Name the blood parasite species.
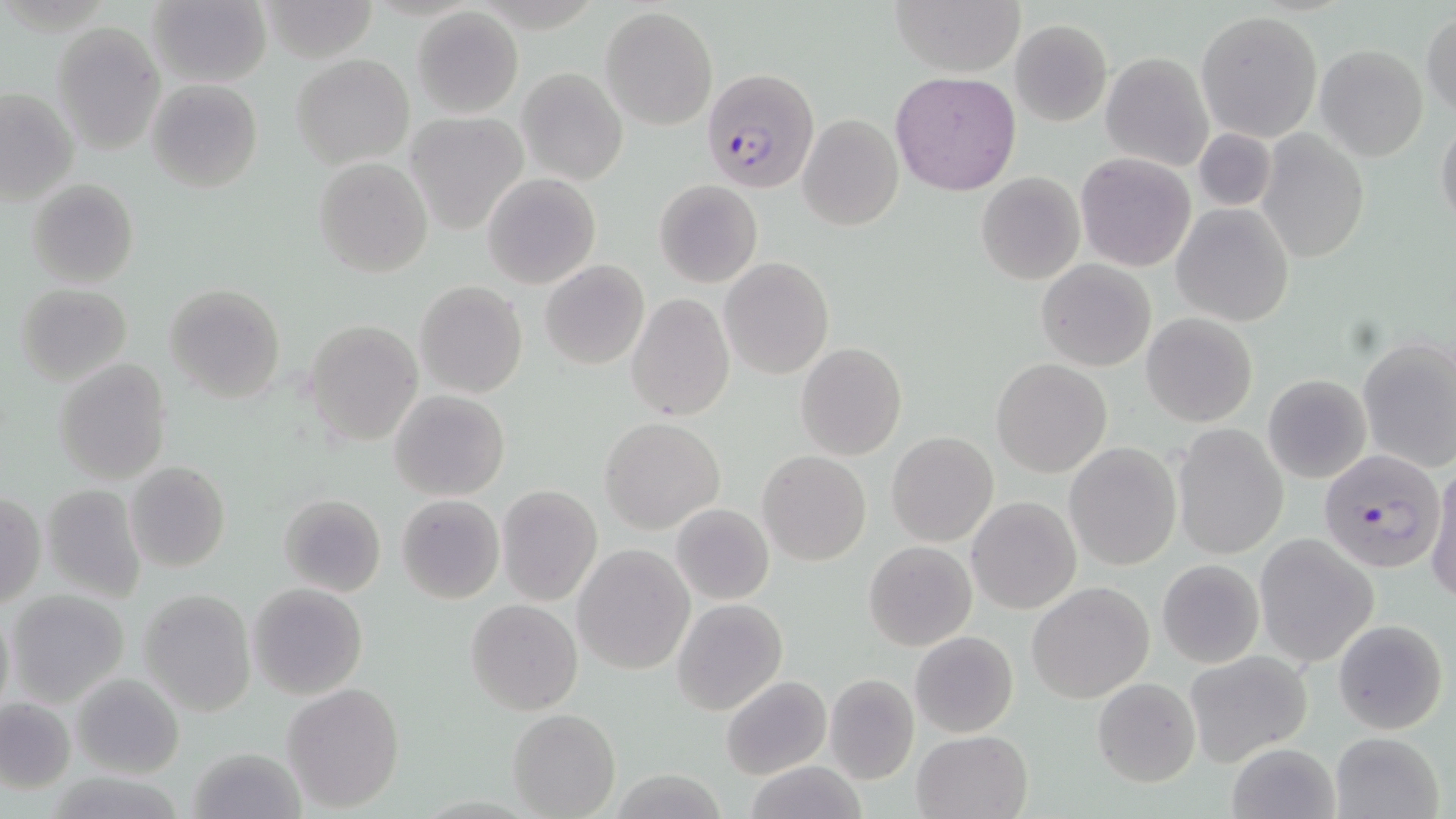
Plasmodium falciparum.

Summary:
  - Coordinate format: approximate bounding boxes as named x1/y1/x2/y2 corners in pixels
  - Uninfected red blood cell locations: (x1=147, y1=0, x2=271, y2=87), (x1=892, y1=0, x2=1023, y2=76), (x1=259, y1=1, x2=381, y2=63), (x1=601, y1=6, x2=717, y2=130), (x1=413, y1=7, x2=523, y2=117), (x1=1196, y1=10, x2=1324, y2=142), (x1=1421, y1=11, x2=1455, y2=119), (x1=1011, y1=18, x2=1112, y2=126), (x1=52, y1=22, x2=165, y2=154), (x1=1315, y1=45, x2=1428, y2=162), (x1=1101, y1=53, x2=1213, y2=171), (x1=293, y1=55, x2=414, y2=169), (x1=518, y1=68, x2=628, y2=184), (x1=890, y1=71, x2=1021, y2=194), (x1=146, y1=79, x2=263, y2=193), (x1=1, y1=87, x2=78, y2=206), (x1=798, y1=112, x2=903, y2=230), (x1=404, y1=113, x2=527, y2=234), (x1=1435, y1=118, x2=1456, y2=234), (x1=1193, y1=129, x2=1276, y2=213), (x1=1257, y1=131, x2=1369, y2=262), (x1=1075, y1=152, x2=1197, y2=273), (x1=314, y1=157, x2=432, y2=276), (x1=976, y1=172, x2=1085, y2=285), (x1=482, y1=174, x2=600, y2=289), (x1=27, y1=178, x2=139, y2=289), (x1=653, y1=180, x2=762, y2=289), (x1=1172, y1=204, x2=1294, y2=327), (x1=719, y1=257, x2=833, y2=381), (x1=1036, y1=258, x2=1156, y2=371), (x1=540, y1=260, x2=649, y2=369), (x1=415, y1=281, x2=527, y2=399), (x1=15, y1=283, x2=133, y2=385), (x1=164, y1=284, x2=286, y2=404), (x1=627, y1=294, x2=734, y2=423), (x1=1140, y1=312, x2=1258, y2=427), (x1=305, y1=318, x2=423, y2=446), (x1=1358, y1=336, x2=1456, y2=473), (x1=795, y1=343, x2=907, y2=460), (x1=53, y1=359, x2=173, y2=484), (x1=992, y1=359, x2=1111, y2=477), (x1=1262, y1=375, x2=1372, y2=484), (x1=390, y1=390, x2=509, y2=500), (x1=600, y1=417, x2=723, y2=533), (x1=1172, y1=423, x2=1288, y2=559), (x1=886, y1=431, x2=998, y2=546), (x1=1065, y1=442, x2=1182, y2=571), (x1=758, y1=451, x2=871, y2=565), (x1=124, y1=461, x2=230, y2=573), (x1=1427, y1=461, x2=1456, y2=605), (x1=41, y1=483, x2=148, y2=601), (x1=496, y1=484, x2=602, y2=606), (x1=1, y1=492, x2=45, y2=609), (x1=279, y1=493, x2=386, y2=596), (x1=397, y1=494, x2=504, y2=603), (x1=968, y1=497, x2=1081, y2=614), (x1=671, y1=503, x2=775, y2=606), (x1=1254, y1=533, x2=1379, y2=668), (x1=864, y1=541, x2=977, y2=651), (x1=574, y1=545, x2=694, y2=674), (x1=1156, y1=559, x2=1265, y2=668), (x1=1026, y1=581, x2=1153, y2=703), (x1=248, y1=582, x2=368, y2=700), (x1=138, y1=587, x2=256, y2=716), (x1=5, y1=590, x2=130, y2=707), (x1=672, y1=598, x2=788, y2=716), (x1=465, y1=599, x2=582, y2=716), (x1=1, y1=600, x2=15, y2=720), (x1=1332, y1=617, x2=1449, y2=736), (x1=911, y1=630, x2=1018, y2=738), (x1=1182, y1=650, x2=1314, y2=766), (x1=71, y1=671, x2=186, y2=778), (x1=823, y1=673, x2=920, y2=784), (x1=721, y1=675, x2=830, y2=779), (x1=1092, y1=678, x2=1202, y2=787), (x1=282, y1=681, x2=404, y2=812), (x1=0, y1=695, x2=76, y2=794), (x1=507, y1=709, x2=621, y2=818), (x1=912, y1=730, x2=1031, y2=818), (x1=1328, y1=730, x2=1445, y2=819), (x1=1228, y1=742, x2=1341, y2=819), (x1=190, y1=745, x2=304, y2=819), (x1=742, y1=761, x2=871, y2=819)
  - Plasmodium falciparum-infected red blood cell locations: (x1=700, y1=66, x2=819, y2=193), (x1=1317, y1=447, x2=1446, y2=576)
  - Modality: light microscopy
  - Image size: 1456×819 pixels
  - Field of view: single
  - Stain: May-Grünwald-Giemsa
  - Preparation: thin blood smear
  - Magnification: 1000x